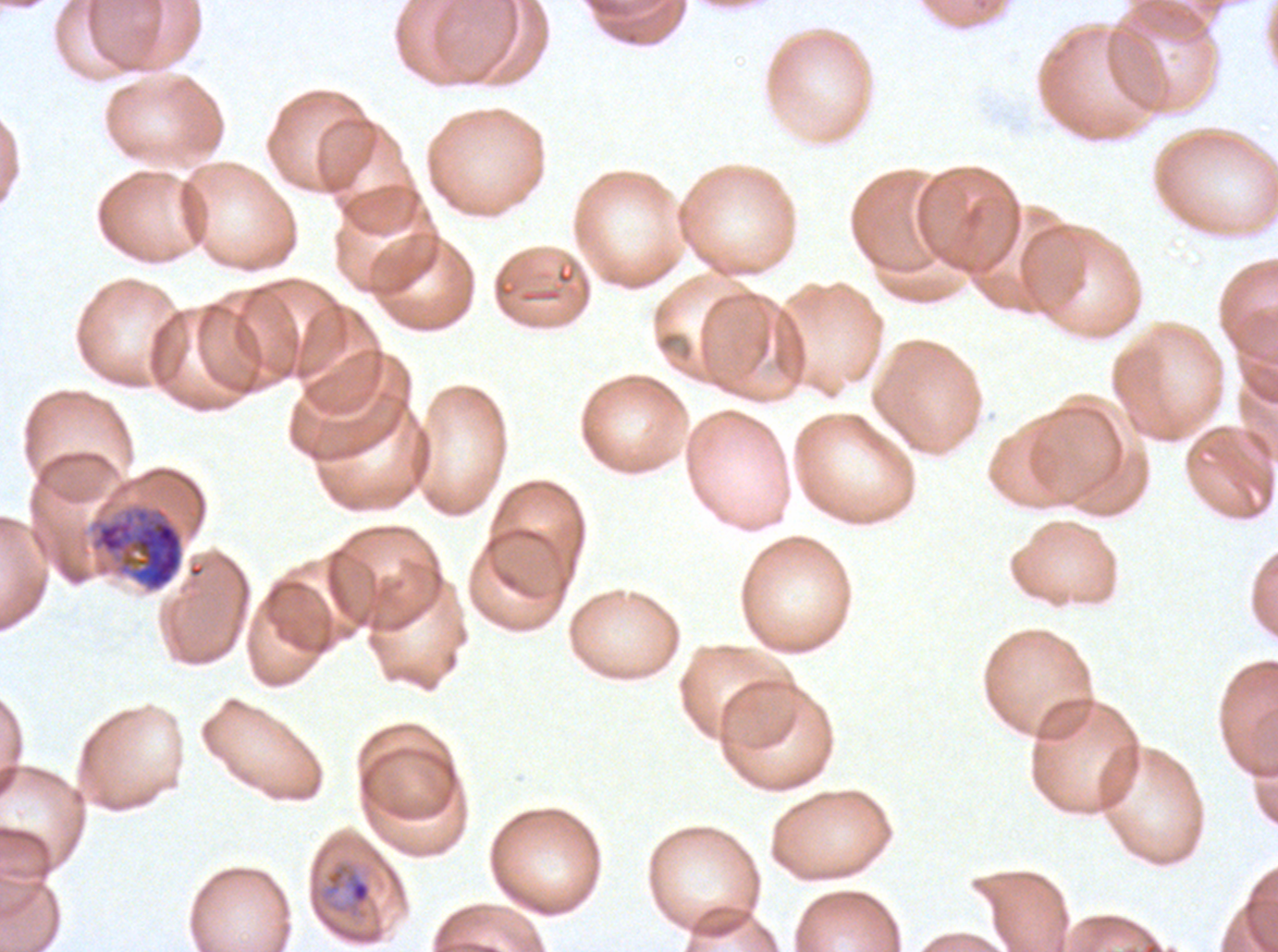
Approximate bounding boxes as {x1, y1, x2, y2} in pixels.
Summary:
  - Early schizont locations: {91, 505, 184, 592}
  - Late-ring/early-trophozoite locations: {318, 860, 373, 919}
  - Preparation: thin blood film
  - Image size: 1278×952 pixels
  - Stain: Giemsa
  - Specimen: P. falciparum from a patient in The Gambia, cultured ex vivo for 24 to 48 hours
  - Field of view: sub-image separated from a larger composite
  - Life-cycle stages observed: late-ring/early-trophozoite, early schizont